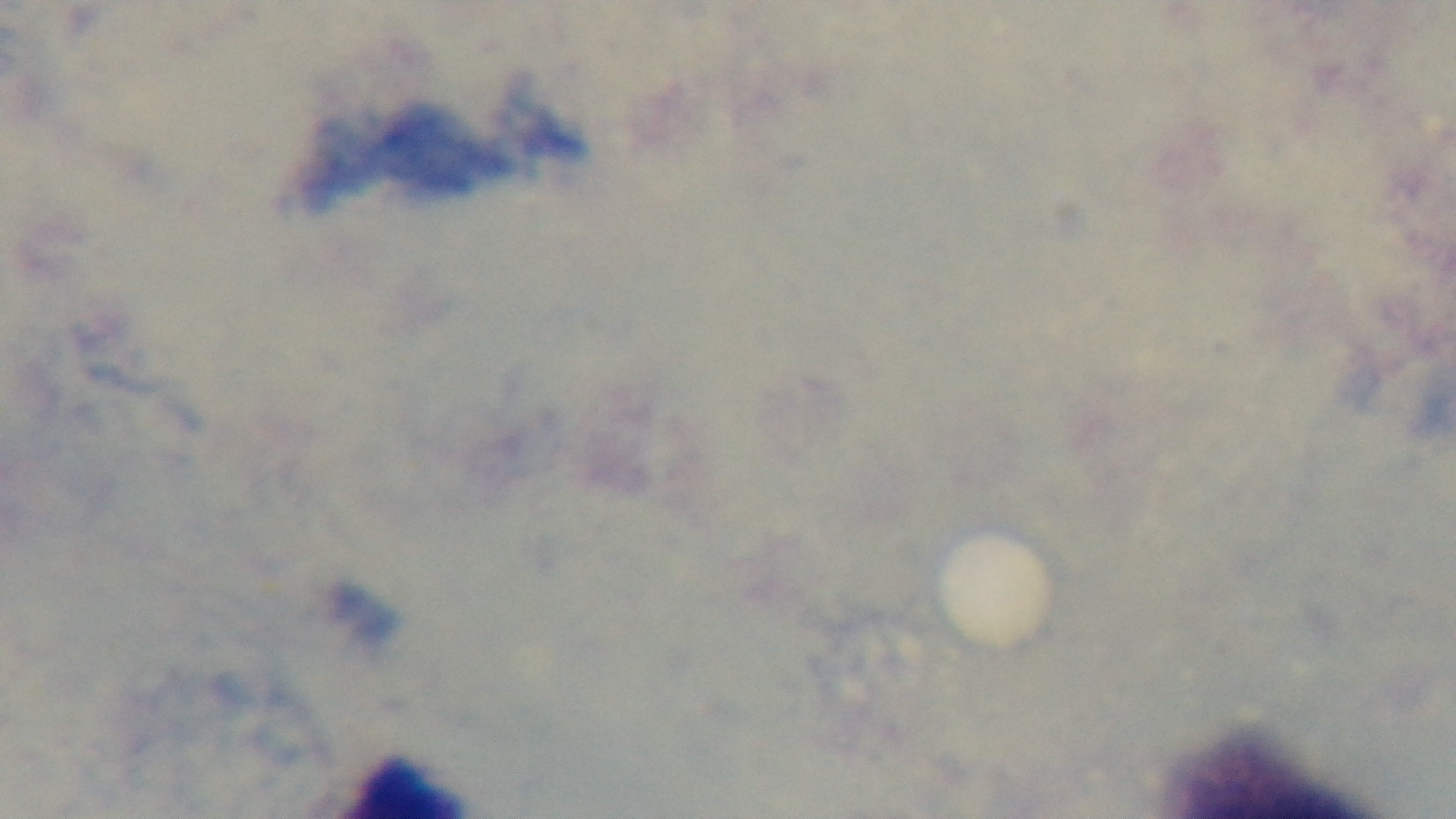
{
  "preparation": "thick",
  "objective": "100x oil immersion",
  "field_of_view": "single",
  "stain": "Giemsa",
  "malaria_status": "negative",
  "capture": "mounted 4K digital camera",
  "modality": "light microscopy"
}